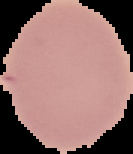

Summary:
  - Result: no Plasmodium parasites detected
  - Preparation: thin blood film
  - Image type: segmented cell region on a black background
  - Image size: 133×154 pixels